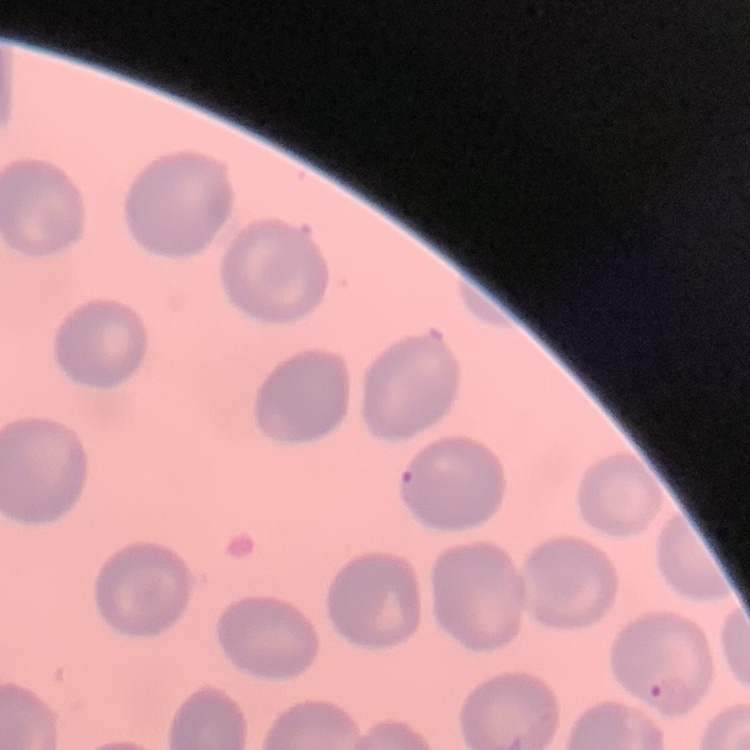

The erythrocytes exhibit no rouleaux formation. Square crop of a larger photomicrograph. Field's or Giemsa stain. Thin blood film.